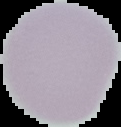

preparation: thin blood film
image_size: 121×127 pixels
result: no Plasmodium parasites seen
image_type: segmented cell region with the area outside set to black